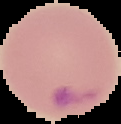
malaria status = parasitized
preparation = thin blood smear
image type = segmented cell region with the area outside set to black
image size = 121×124 pixels